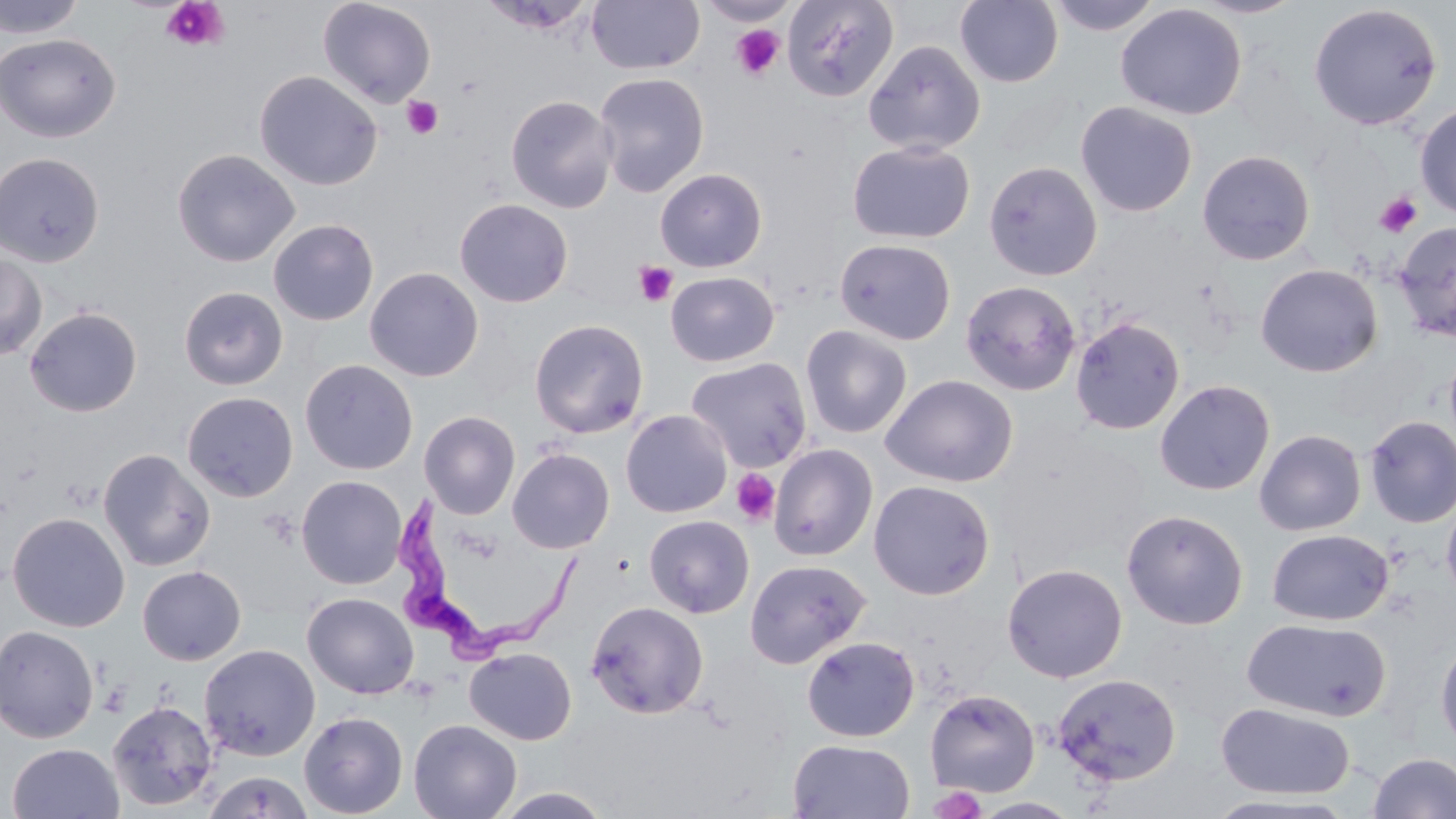

Approximate bounding boxes as (x1,y1)-(x2,y2) corner pairs in pixels. Trypanosoma brucei locations: (391,494)-(583,670). Uninfected red blood cell locations: (0,0)-(87,39), (318,0)-(437,108), (585,0)-(705,74), (698,0)-(798,27), (782,0)-(898,102), (955,0)-(1063,87), (1046,0)-(1164,36), (1187,0)-(1307,19), (1116,3)-(1247,120), (1308,3)-(1443,130), (0,32)-(121,144), (863,39)-(986,156), (254,70)-(382,190), (593,72)-(709,197), (505,94)-(618,214), (1075,101)-(1198,217), (1415,102)-(1456,219), (847,140)-(976,244), (172,148)-(300,267), (1196,149)-(1316,266), (0,152)-(105,268), (983,160)-(1103,282), (655,168)-(767,272), (454,198)-(574,308), (268,218)-(379,326), (1393,221)-(1456,342), (834,238)-(956,345), (0,252)-(47,362), (1255,263)-(1383,377), (364,267)-(484,382), (665,271)-(779,366), (960,280)-(1081,396), (179,286)-(288,390), (24,306)-(143,417), (1070,316)-(1185,436), (529,318)-(649,438), (800,325)-(913,439), (1444,344)-(1456,456), (685,357)-(812,472), (300,359)-(418,475), (880,374)-(1018,487), (1154,379)-(1275,495), (182,391)-(298,502), (621,409)-(732,518), (419,410)-(520,519), (1364,415)-(1456,528), (1254,429)-(1366,536), (769,443)-(878,562), (99,448)-(215,572), (507,448)-(615,554), (296,475)-(407,589), (868,480)-(995,600), (1441,491)-(1456,609), (1121,509)-(1249,630), (7,512)-(130,632), (643,514)-(754,618), (1267,529)-(1393,626), (744,558)-(870,669), (1002,563)-(1127,683), (137,566)-(246,665), (302,592)-(419,699), (585,600)-(709,719), (1242,618)-(1391,722), (0,625)-(100,743), (1435,635)-(1456,755), (802,636)-(920,742), (199,644)-(321,761), (464,647)-(577,744), (1052,672)-(1181,786), (925,689)-(1041,796), (107,699)-(219,812), (1216,703)-(1355,800), (299,711)-(408,818), (408,718)-(522,819), (787,739)-(916,819), (7,743)-(124,819), (1367,752)-(1456,819), (202,770)-(314,819), (493,787)-(615,818), (1202,794)-(1355,818), (972,797)-(1082,818). Platelet locations: (161,0)-(230,52), (730,25)-(785,80), (402,95)-(443,139), (1374,192)-(1423,238), (634,260)-(678,307), (731,468)-(780,527), (929,785)-(985,819). Slide-level diagnosis: Trypanosoma brucei. Optical microscopy. Single field of view. Thin blood film. May-Grünwald-Giemsa stain. Captured at 1000x magnification. Image is 1456×819 pixels.